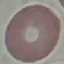

result = no malaria parasites seen
preparation = thin blood film
stain = Giemsa
capture = smartphone through the microscope eyepiece
image type = cell patch, automatically extracted from a larger field of view and resized to 64 × 64 pixels